Assess this cell for malaria.
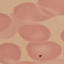
It is uninfected.

capture: smartphone through the microscope eyepiece
stain: Giemsa
image_type: automatically extracted cell patch, resized to 64 × 64 pixels
preparation: thin blood smear